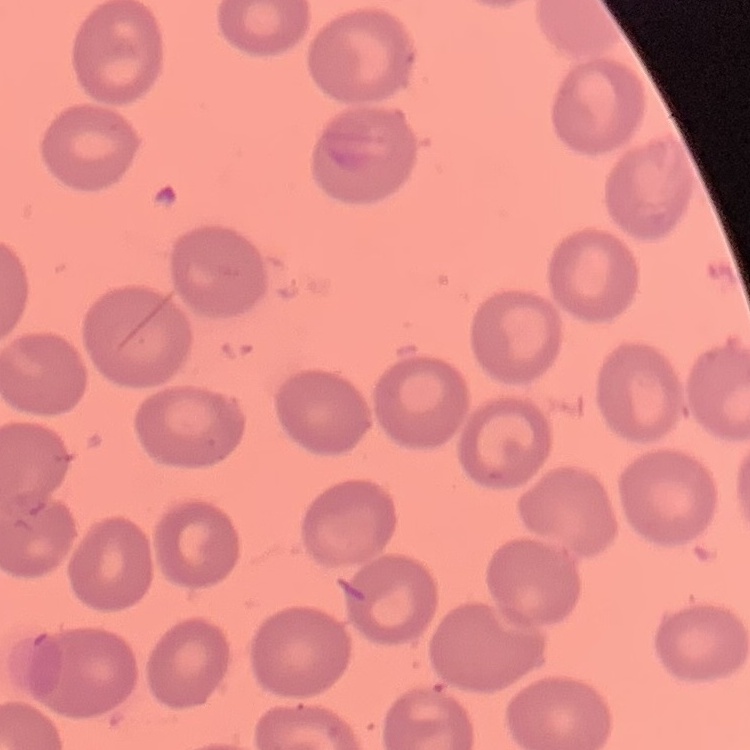
{
  "erythrocyte_morphology": "no rouleaux formation",
  "preparation": "thin peripheral smear",
  "stain": "Field's or Giemsa",
  "image_type": "square crop of a larger photomicrograph"
}